Report the malaria status of this cell.
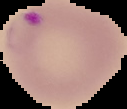

Parasitized.

Summary:
  - Preparation: thin blood film
  - Image size: 127×109 pixels
  - Image type: cell region segmented out of the field of view; surrounding area masked to black